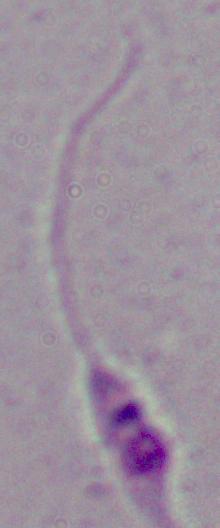
magnification = 1000x
modality = micrograph
identification = Leishmania